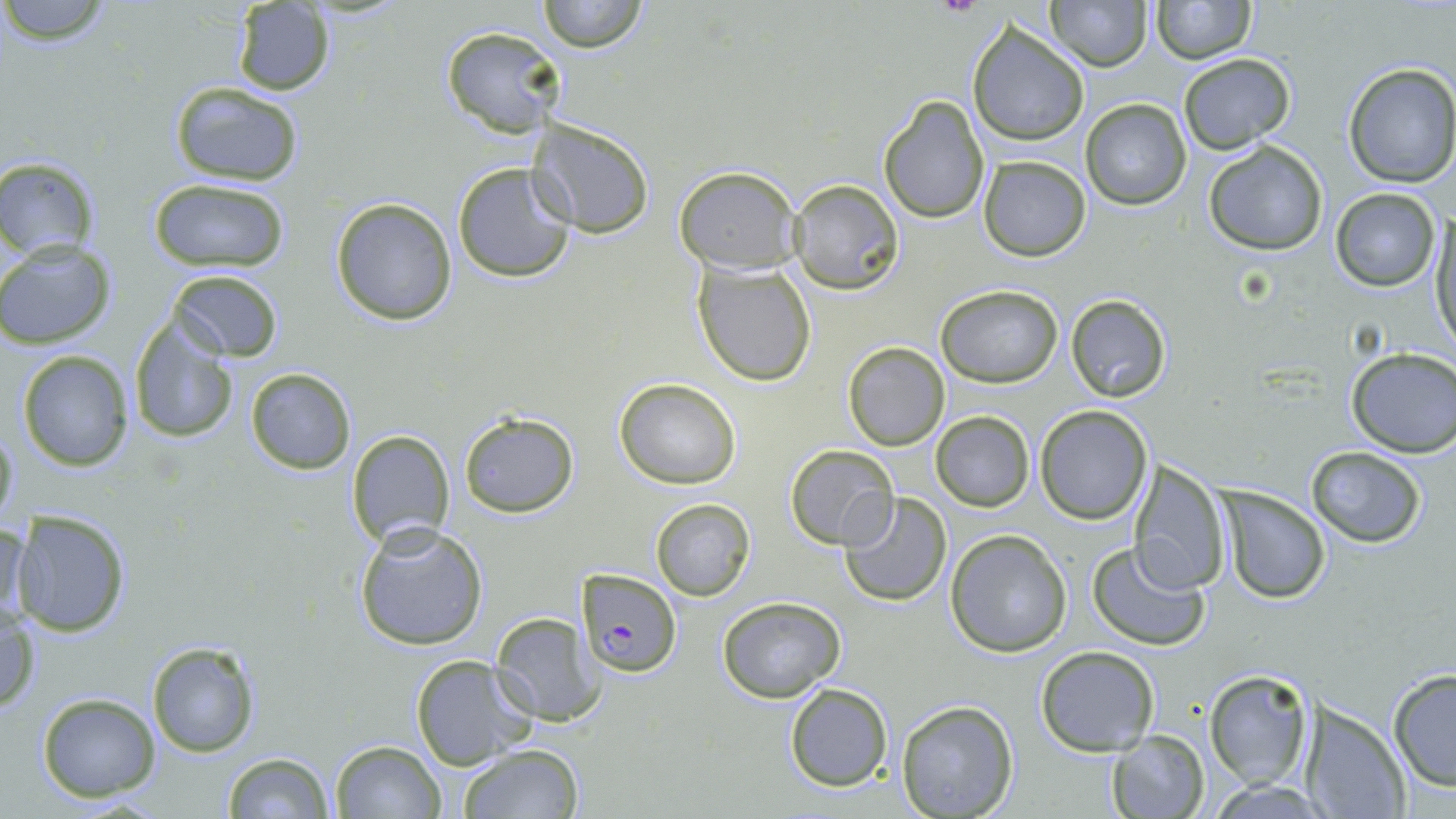
{
  "slide_level_diagnosis": "Plasmodium falciparum",
  "stain": "May-Grünwald-Giemsa",
  "magnification": "1000x",
  "field_of_view": "single",
  "uninfected_red_blood_cell_locations": "approximate bounding boxes as named x1/y1/x2/y2 corners in pixels: (x1=1, y1=0, x2=114, y2=45), (x1=534, y1=0, x2=652, y2=53), (x1=1151, y1=0, x2=1255, y2=62), (x1=230, y1=1, x2=336, y2=96), (x1=1048, y1=1, x2=1151, y2=71), (x1=966, y1=23, x2=1090, y2=147), (x1=440, y1=24, x2=565, y2=140), (x1=1178, y1=52, x2=1295, y2=152), (x1=1340, y1=62, x2=1456, y2=187), (x1=169, y1=81, x2=305, y2=187), (x1=877, y1=94, x2=990, y2=225), (x1=1080, y1=98, x2=1192, y2=211), (x1=528, y1=118, x2=655, y2=236), (x1=1203, y1=140, x2=1329, y2=256), (x1=0, y1=156, x2=100, y2=262), (x1=979, y1=156, x2=1091, y2=262), (x1=451, y1=160, x2=579, y2=284), (x1=673, y1=166, x2=801, y2=274), (x1=146, y1=178, x2=290, y2=271), (x1=788, y1=179, x2=905, y2=295), (x1=1331, y1=187, x2=1441, y2=293), (x1=329, y1=198, x2=458, y2=325), (x1=1430, y1=212, x2=1455, y2=350), (x1=0, y1=241, x2=117, y2=349), (x1=693, y1=261, x2=818, y2=387), (x1=168, y1=270, x2=284, y2=361), (x1=135, y1=275, x2=273, y2=419), (x1=934, y1=285, x2=1064, y2=387), (x1=1064, y1=292, x2=1173, y2=404), (x1=126, y1=319, x2=239, y2=445), (x1=842, y1=342, x2=950, y2=451), (x1=15, y1=348, x2=136, y2=471), (x1=1345, y1=348, x2=1456, y2=457), (x1=244, y1=366, x2=356, y2=475), (x1=614, y1=378, x2=741, y2=489), (x1=1034, y1=405, x2=1153, y2=524), (x1=930, y1=411, x2=1034, y2=511), (x1=459, y1=412, x2=579, y2=517), (x1=0, y1=414, x2=18, y2=529), (x1=347, y1=428, x2=456, y2=549), (x1=785, y1=443, x2=899, y2=551), (x1=1305, y1=446, x2=1428, y2=548), (x1=1129, y1=461, x2=1231, y2=594), (x1=1218, y1=489, x2=1330, y2=604), (x1=838, y1=494, x2=954, y2=606), (x1=650, y1=499, x2=755, y2=600), (x1=8, y1=510, x2=133, y2=639), (x1=1, y1=516, x2=32, y2=629), (x1=353, y1=523, x2=489, y2=652), (x1=946, y1=529, x2=1073, y2=657), (x1=1087, y1=540, x2=1211, y2=651), (x1=718, y1=596, x2=845, y2=702), (x1=1, y1=609, x2=41, y2=714), (x1=488, y1=609, x2=605, y2=727), (x1=146, y1=641, x2=261, y2=758), (x1=1036, y1=646, x2=1160, y2=754), (x1=409, y1=655, x2=537, y2=770), (x1=1386, y1=668, x2=1456, y2=792), (x1=1204, y1=669, x2=1314, y2=791), (x1=783, y1=682, x2=894, y2=793), (x1=36, y1=693, x2=161, y2=803), (x1=895, y1=700, x2=1019, y2=818), (x1=1299, y1=701, x2=1411, y2=819), (x1=1106, y1=732, x2=1209, y2=817), (x1=331, y1=739, x2=447, y2=818), (x1=459, y1=744, x2=582, y2=819), (x1=220, y1=751, x2=335, y2=819), (x1=1207, y1=778, x2=1329, y2=817)",
  "preparation": "thin blood film",
  "image_size": "1456×819 pixels",
  "plasmodium_falciparum_infected_red_blood_cell_locations": "approximate bounding boxes as named x1/y1/x2/y2 corners in pixels: (x1=577, y1=570, x2=682, y2=677)",
  "modality": "optical microscopy"
}